Identify the preparation type.
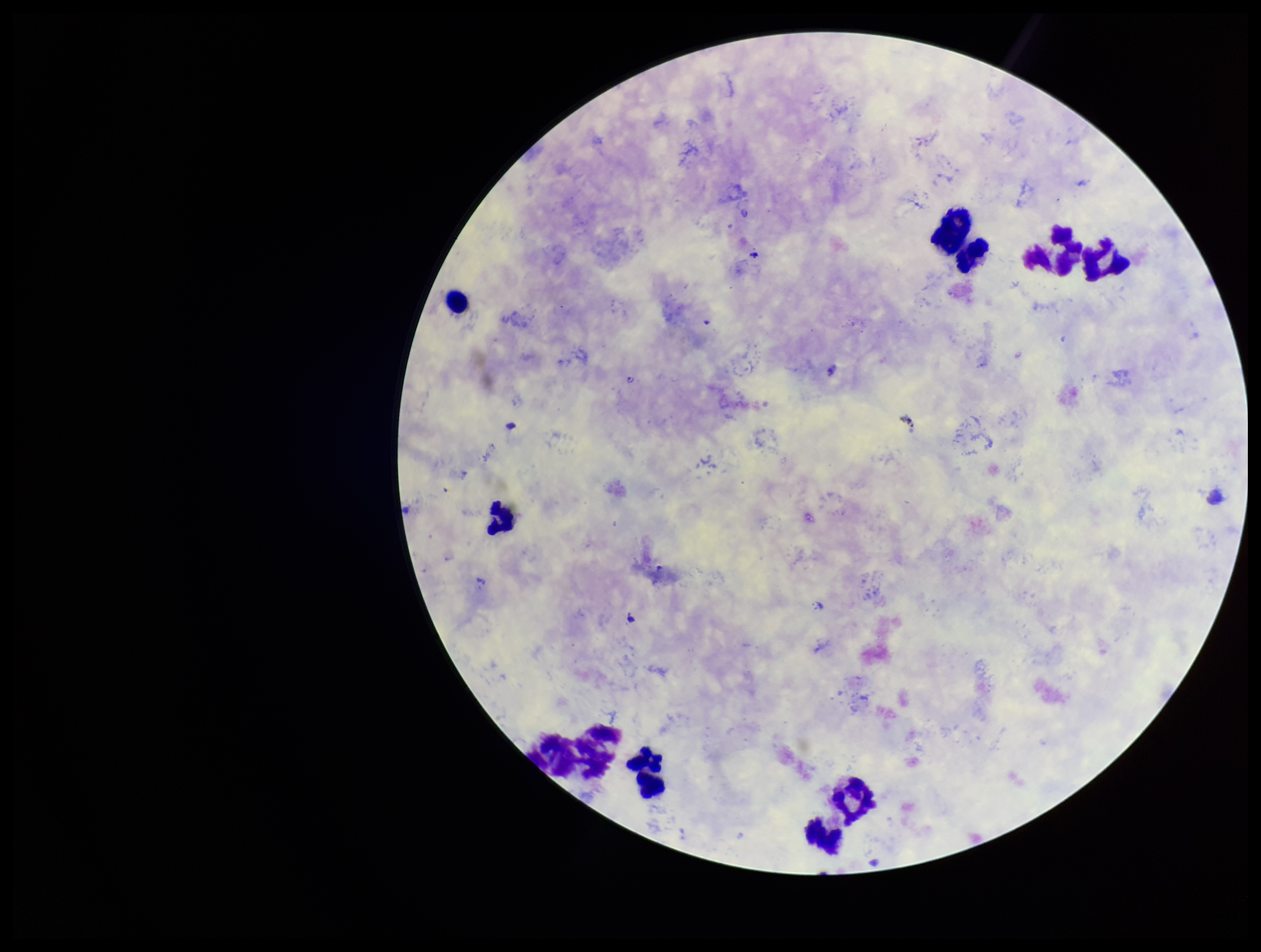
Thick.

capture = smartphone photograph through the microscope eyepiece
field of view = one from this slide
leukocyte count = 11
stain = Giemsa
Plasmodium parasites = none seen
patient malaria status = infected
parasite count = 0
species reported for this patient = Plasmodium vivax
image size = 1261×952 pixels